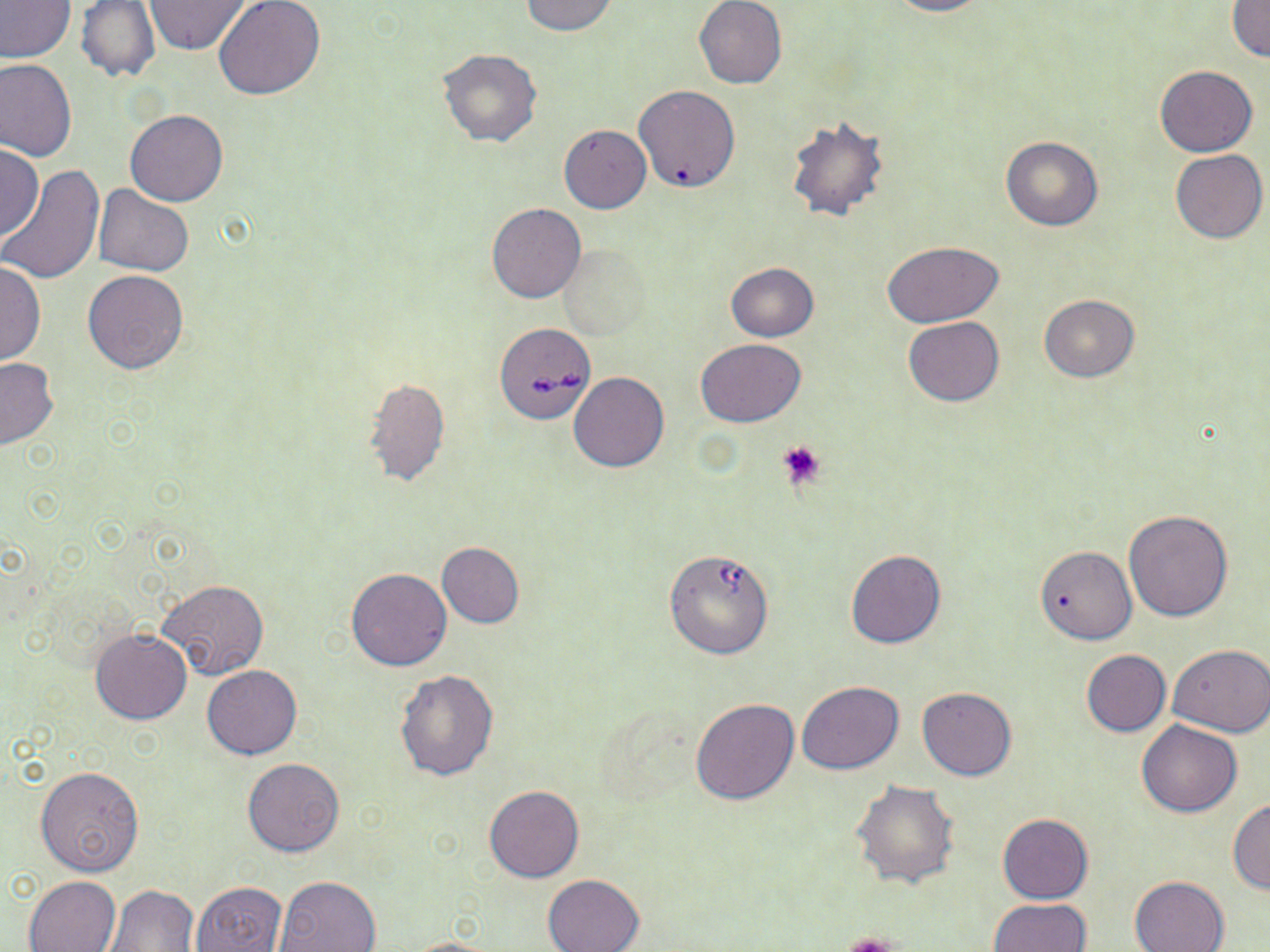

{
  "slide_level_diagnosis": "Babesia divergens",
  "magnification": "1000x",
  "preparation": "thin blood smear",
  "platelet_locations": "approximate bounding boxes as (x1,y1)-(x2,y2) corner pairs in pixels: (776,439)-(825,491), (840,932)-(899,952)",
  "stain": "May-Grünwald-Giemsa",
  "uninfected_red_blood_cell_locations": "approximate bounding boxes as (x1,y1)-(x2,y2) corner pairs in pixels: (0,0)-(75,62), (213,0)-(325,101), (521,0)-(618,36), (693,0)-(788,89), (885,0)-(992,17), (73,1)-(162,84), (143,1)-(251,54), (1228,2)-(1270,63), (437,48)-(543,148), (0,56)-(77,160), (1155,65)-(1256,156), (634,84)-(740,193), (125,109)-(228,207), (784,113)-(891,222), (559,125)-(651,214), (1000,137)-(1103,231), (0,144)-(44,240), (1170,148)-(1267,243), (0,165)-(106,285), (93,185)-(195,276), (486,202)-(586,304), (882,240)-(1004,325), (559,245)-(650,340), (0,259)-(45,367), (725,262)-(818,342), (83,270)-(189,374), (1039,294)-(1140,382), (903,317)-(1005,406), (695,339)-(805,426), (0,356)-(57,448), (568,372)-(669,472), (363,377)-(449,487), (1124,509)-(1234,622), (436,541)-(524,628), (1034,545)-(1137,644), (844,550)-(947,649), (346,567)-(452,671), (157,580)-(270,681), (90,629)-(192,725), (1166,644)-(1269,737), (1079,650)-(1172,737), (201,665)-(301,758), (394,667)-(499,781), (797,681)-(904,773), (917,686)-(1019,781), (690,697)-(800,805), (1136,719)-(1243,817), (241,757)-(344,856), (36,766)-(144,876), (851,779)-(960,889), (484,784)-(585,883), (1228,798)-(1270,893), (997,814)-(1093,903), (541,872)-(645,952), (24,875)-(121,951), (273,875)-(381,951), (1129,875)-(1230,952), (191,881)-(288,952), (105,884)-(200,951), (988,898)-(1092,952), (403,936)-(507,951)",
  "babesia_divergens_infected_red_blood_cell_locations": "approximate bounding boxes as (x1,y1)-(x2,y2) corner pairs in pixels: (493,322)-(597,424), (663,552)-(770,659)",
  "modality": "optical microscopy",
  "field_of_view": "single",
  "image_size": "1270×952 pixels"
}